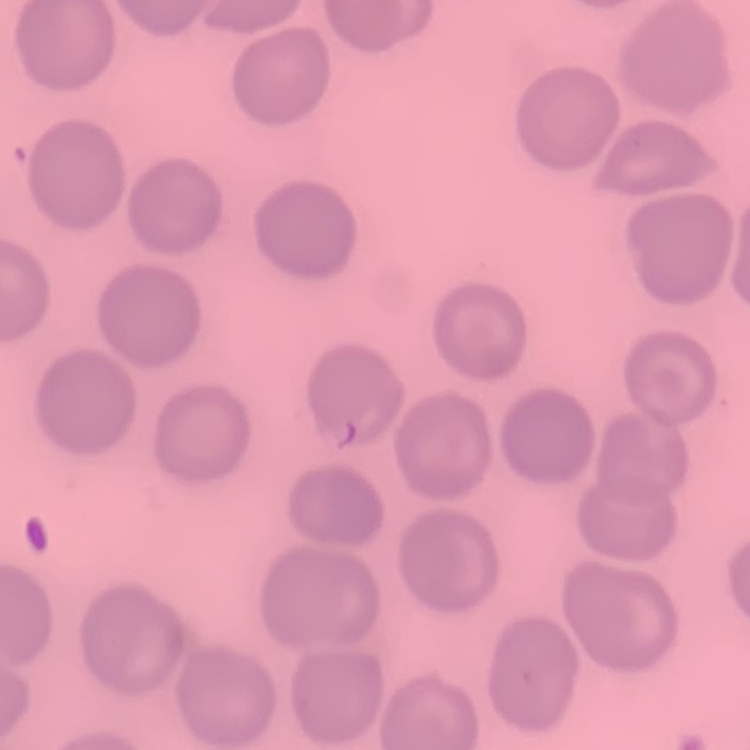
The red blood cells show no rouleaux formation. Thin peripheral smear. Square crop of a larger photomicrograph. Field's or Giemsa stain.